Locate every malaria parasite.
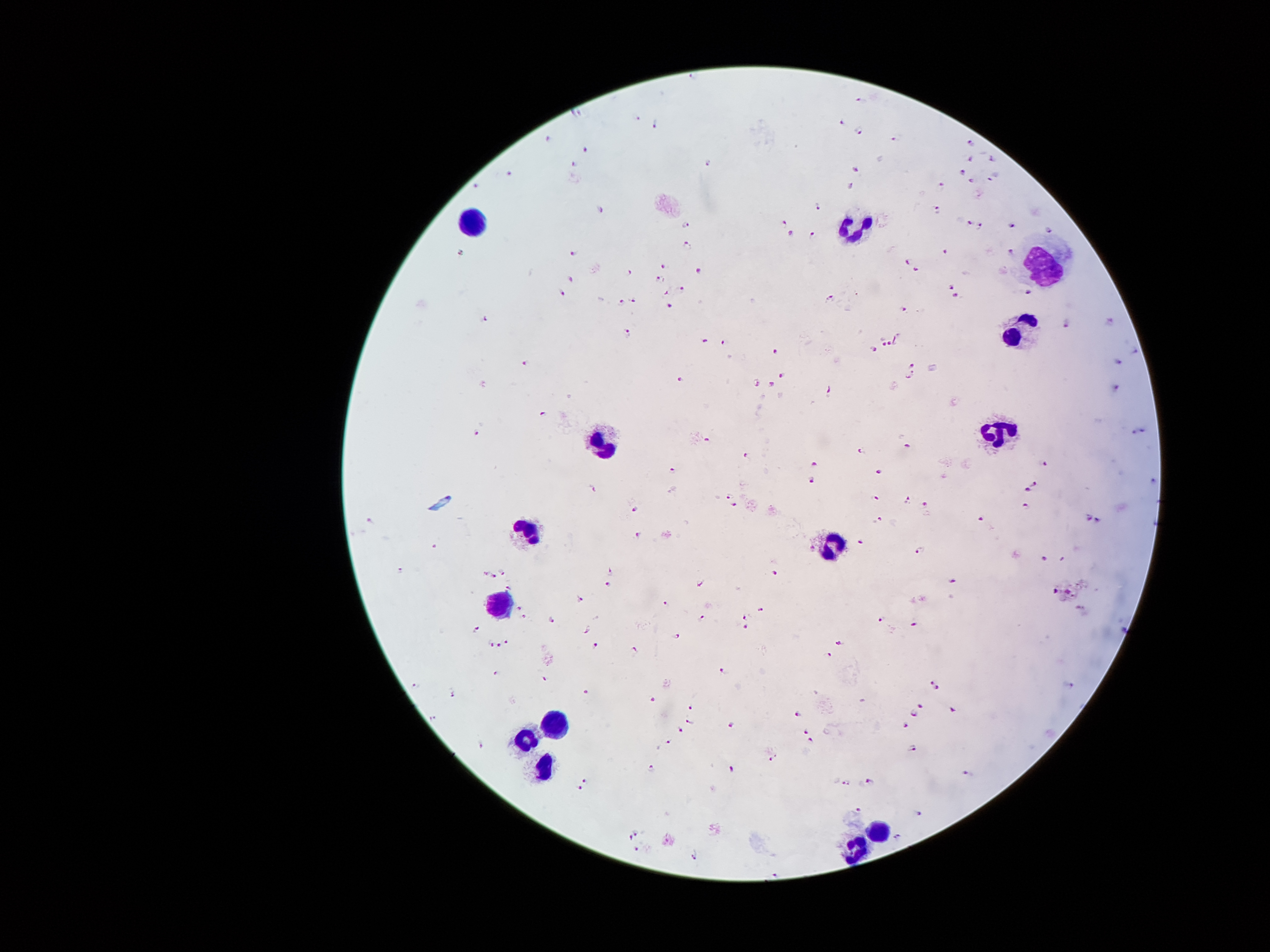
Approximate centers as {x, y} in pixels.
Malaria parasites: {694, 75}, {861, 97}, {576, 111}, {638, 115}, {655, 122}, {839, 122}, {858, 129}, {550, 137}, {891, 139}, {973, 141}, {583, 147}, {970, 159}, {993, 159}, {576, 162}, {708, 162}, {856, 169}, {961, 169}, {510, 173}, {993, 176}, {970, 180}, {941, 184}, {476, 185}, {851, 188}, {818, 206}, {937, 209}, {601, 211}, {786, 221}, {969, 222}, {689, 225}, {979, 225}, {1012, 226}, {1050, 230}, {791, 231}, {811, 232}, {689, 245}, {1011, 249}, {574, 250}, {946, 250}, {460, 253}, {909, 263}, {664, 267}, {699, 271}, {917, 271}, {628, 272}, {571, 278}, {658, 279}, {951, 286}, {683, 288}, {666, 291}, {1029, 291}, {563, 292}, {955, 293}, {630, 297}, {829, 298}, {622, 301}, {670, 304}, {905, 311}, {484, 319}, {1109, 323}, {1066, 324}, {627, 329}, {896, 339}, {703, 342}, {723, 343}, {880, 343}, {889, 343}, {874, 349}, {777, 352}, {1134, 352}, {524, 362}, {1119, 362}, {913, 365}, {782, 375}, {910, 376}, {679, 380}, {755, 381}, {772, 384}, {1115, 386}, {828, 389}, {543, 410}, {1146, 427}, {476, 432}, {1133, 432}, {707, 438}, {909, 444}, {860, 449}, {748, 456}, {1045, 461}, {814, 463}, {671, 469}, {881, 472}, {812, 478}, {1155, 478}, {1033, 480}, {594, 488}, {1029, 491}, {728, 494}, {876, 497}, {907, 501}, {924, 503}, {1026, 503}, {735, 506}, {634, 508}, {1089, 516}, {982, 517}, {1099, 517}, {879, 519}, {370, 520}, {639, 531}, {857, 540}, {434, 545}, {921, 549}, {1043, 558}, {400, 569}, {773, 569}, {484, 572}, {503, 572}, {609, 572}, {493, 576}, {951, 581}, {700, 582}, {608, 583}, {508, 586}, {1057, 589}, {1070, 591}, {580, 599}, {665, 601}, {518, 605}, {762, 610}, {1080, 610}, {524, 615}, {745, 617}, {702, 618}, {880, 618}, {552, 622}, {914, 624}, {746, 627}, {1122, 627}, {586, 628}, {476, 631}, {676, 634}, {506, 641}, {837, 641}, {492, 643}, {595, 643}, {499, 645}, {633, 651}, {829, 655}, {496, 670}, {722, 671}, {543, 678}, {931, 683}, {417, 685}, {1070, 687}, {936, 689}, {585, 692}, {452, 693}, {653, 699}, {690, 706}, {922, 706}, {800, 712}, {955, 712}, {916, 713}, {433, 718}, {689, 720}, {731, 723}, {907, 725}, {681, 730}, {805, 731}, {810, 740}, {667, 741}, {480, 744}, {913, 748}, {772, 759}, {731, 767}, {650, 770}, {965, 773}, {871, 779}, {586, 781}, {846, 782}, {580, 787}, {857, 807}, {919, 814}, {636, 833}, {898, 835}, {629, 838}, {637, 849}, {697, 856}, {776, 872}.

Leukocyte locations: {466, 221}, {857, 230}, {1041, 266}, {1022, 327}, {999, 431}, {605, 437}, {527, 534}, {834, 547}, {498, 608}, {553, 722}, {520, 741}, {540, 773}, {876, 828}, {853, 851}. Thick blood smear. 100x magnification. Patient malaria status: infected with Plasmodium falciparum. Image is 1270×952 pixels. Photographed through the microscope eyepiece with a smartphone camera. Single field of view. Giemsa stain.